Classify this cell by malaria status.
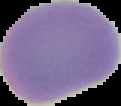
It is uninfected.

image_size: 121×106 pixels
image_type: segmented cell region on a black background
preparation: thin blood film